Name the parasite shown.
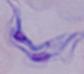

A trypanosome.

magnification = 1000x
modality = photomicrograph